Report the malaria status of this cell.
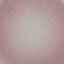

Uninfected.

Thin blood smear. Acquired by smartphone through the microscope eyepiece. Cell patch, automatically extracted from a larger field of view and resized to 64 × 64 pixels. Giemsa-stained preparation.